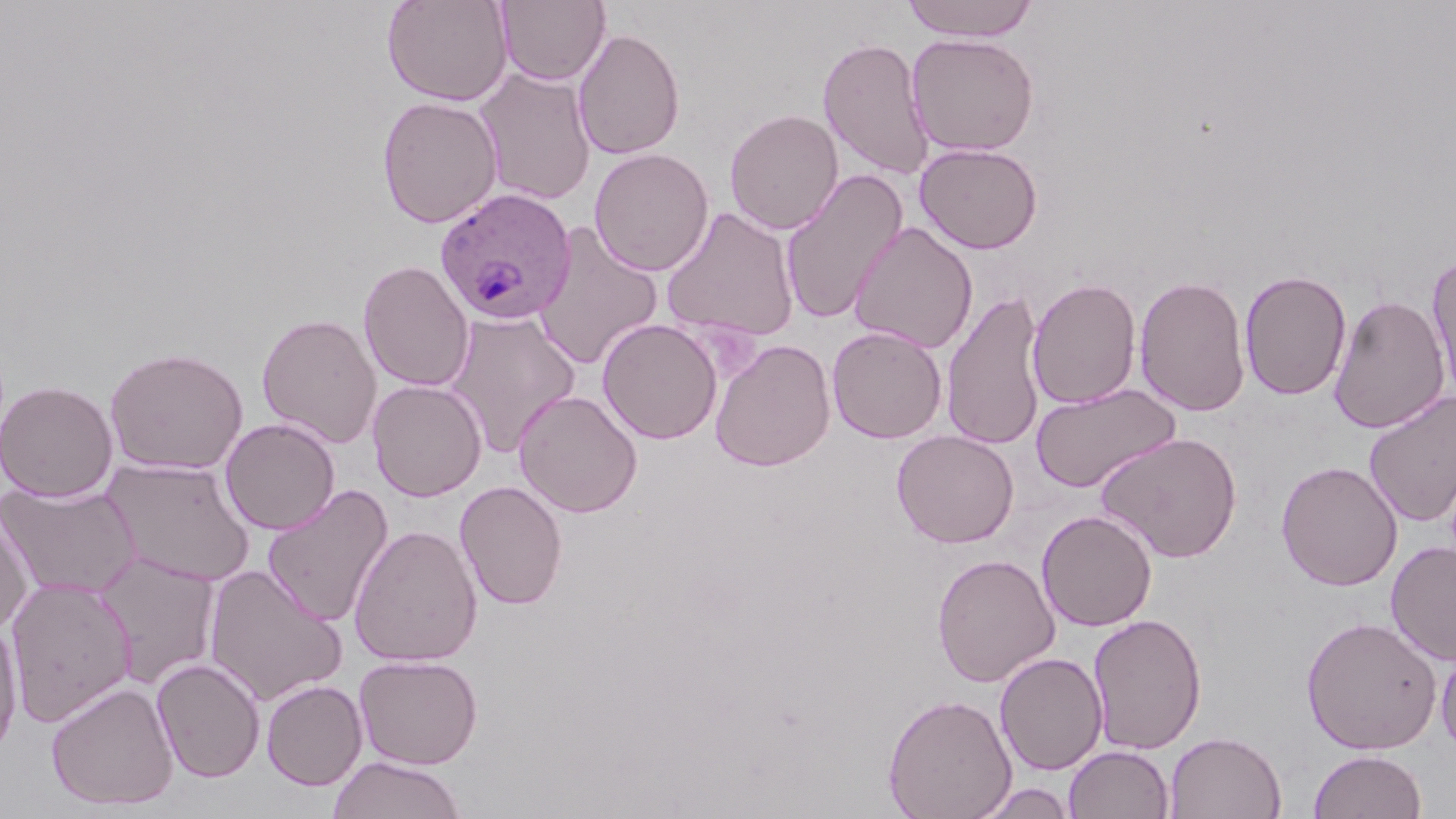
{
  "slide_level_diagnosis": "Plasmodium ovale",
  "preparation": "thin blood smear",
  "magnification": "1000x",
  "stain": "May-Grünwald-Giemsa",
  "modality": "optical microscopy",
  "uninfected_red_blood_cell_locations": "approximate bounding boxes as named x1/y1/x2/y2 corners in pixels: (x1=382, y1=0, x2=513, y2=106), (x1=496, y1=0, x2=611, y2=86), (x1=902, y1=1, x2=1040, y2=42), (x1=573, y1=27, x2=685, y2=160), (x1=906, y1=32, x2=1040, y2=157), (x1=818, y1=36, x2=934, y2=180), (x1=475, y1=67, x2=597, y2=206), (x1=376, y1=96, x2=503, y2=228), (x1=724, y1=108, x2=844, y2=235), (x1=914, y1=142, x2=1043, y2=254), (x1=589, y1=148, x2=714, y2=276), (x1=780, y1=169, x2=908, y2=325), (x1=661, y1=207, x2=800, y2=344), (x1=848, y1=221, x2=978, y2=353), (x1=533, y1=223, x2=664, y2=372), (x1=1426, y1=252, x2=1456, y2=404), (x1=358, y1=259, x2=475, y2=392), (x1=1239, y1=269, x2=1352, y2=401), (x1=1134, y1=274, x2=1251, y2=417), (x1=1027, y1=277, x2=1142, y2=409), (x1=941, y1=289, x2=1047, y2=452), (x1=1328, y1=294, x2=1450, y2=435), (x1=445, y1=311, x2=581, y2=456), (x1=257, y1=313, x2=382, y2=447), (x1=597, y1=318, x2=723, y2=444), (x1=827, y1=325, x2=947, y2=443), (x1=710, y1=339, x2=836, y2=472), (x1=104, y1=346, x2=250, y2=475), (x1=1, y1=379, x2=118, y2=501), (x1=367, y1=379, x2=487, y2=501), (x1=1031, y1=382, x2=1180, y2=494), (x1=513, y1=389, x2=643, y2=517), (x1=1363, y1=391, x2=1456, y2=528), (x1=220, y1=417, x2=340, y2=535), (x1=891, y1=429, x2=1019, y2=548), (x1=1095, y1=431, x2=1243, y2=563), (x1=101, y1=458, x2=256, y2=587), (x1=1276, y1=460, x2=1403, y2=591), (x1=1, y1=480, x2=140, y2=601), (x1=454, y1=480, x2=568, y2=610), (x1=261, y1=484, x2=394, y2=627), (x1=1036, y1=509, x2=1158, y2=632), (x1=0, y1=510, x2=35, y2=634), (x1=348, y1=524, x2=483, y2=666), (x1=1386, y1=541, x2=1456, y2=666), (x1=92, y1=551, x2=222, y2=689), (x1=931, y1=553, x2=1060, y2=687), (x1=202, y1=563, x2=348, y2=706), (x1=5, y1=577, x2=137, y2=727), (x1=1087, y1=613, x2=1207, y2=755), (x1=1300, y1=615, x2=1443, y2=754), (x1=0, y1=618, x2=24, y2=755), (x1=1436, y1=642, x2=1456, y2=759), (x1=994, y1=652, x2=1108, y2=775), (x1=354, y1=654, x2=483, y2=770), (x1=152, y1=657, x2=266, y2=783), (x1=261, y1=679, x2=367, y2=790), (x1=46, y1=680, x2=179, y2=811), (x1=882, y1=693, x2=1017, y2=819), (x1=1165, y1=731, x2=1287, y2=819), (x1=1063, y1=745, x2=1174, y2=819), (x1=1308, y1=750, x2=1427, y2=819), (x1=327, y1=755, x2=465, y2=819), (x1=972, y1=782, x2=1078, y2=819)",
  "field_of_view": "single",
  "plasmodium_ovale_infected_red_blood_cell_locations": "approximate bounding boxes as named x1/y1/x2/y2 corners in pixels: (x1=434, y1=187, x2=578, y2=326)",
  "image_size": "1456×819 pixels"
}